Report the malaria status of this cell.
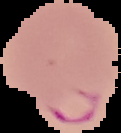
It is parasitized.

Cell region segmented out of the field of view; the surrounding area is masked to black. From a thin blood film. Image is 121×133 pixels.